Assess this cell for malaria.
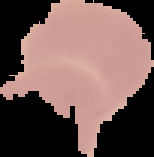
It is uninfected.

image type = segmented cell region on a black background
image size = 154×157 pixels
preparation = thin blood smear